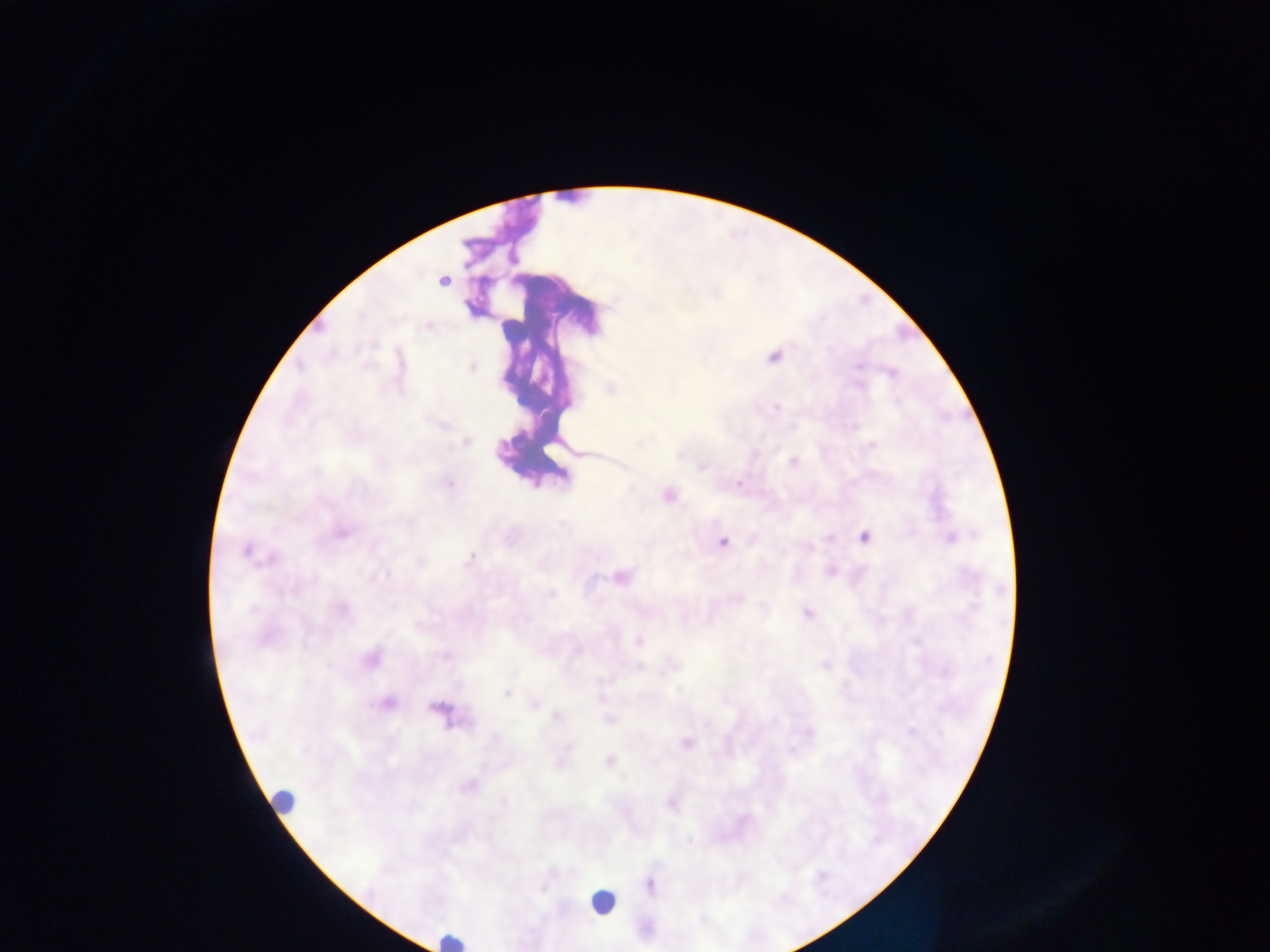
country = Ghana
preparation = thick blood film
field of view = single
image size = 1270×952 pixels
capture = mobile-phone photograph through a microscope
Plasmodium parasite locations = approximate centers as [x, y] in pixels: [442, 281], [716, 293], [428, 327], [774, 357], [859, 366], [472, 367], [892, 373], [504, 383], [859, 385], [610, 388], [776, 407], [466, 442], [641, 442], [871, 445], [680, 455], [793, 462], [703, 466], [315, 472], [449, 483], [738, 484], [669, 495], [563, 526], [341, 532], [864, 537], [950, 538], [828, 539], [723, 543], [246, 551], [471, 557], [273, 559], [419, 562], [830, 570], [386, 574], [621, 577], [550, 595], [343, 609], [807, 613], [638, 641], [577, 650], [446, 657], [370, 660], [328, 666], [824, 666], [637, 667], [507, 693], [599, 698], [388, 704], [534, 704], [557, 717], [609, 720], [809, 731], [911, 732], [687, 744], [568, 746], [609, 761], [560, 763], [469, 786], [670, 804], [689, 841], [649, 885], [542, 889]
leukocyte locations = approximate centers as [x, y] in pixels: [283, 800], [603, 902], [452, 940]